Comment on the morphology of the erythrocytes.
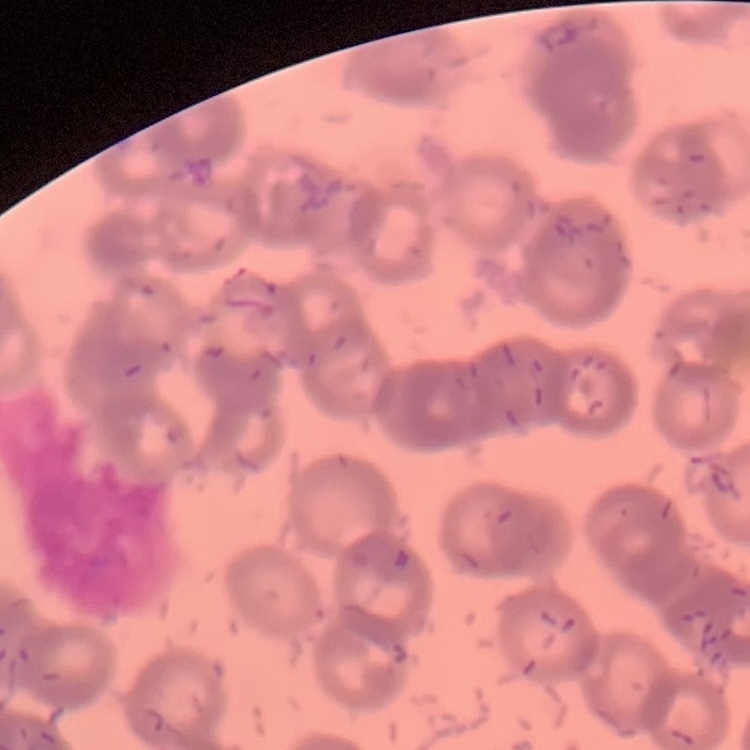
They show rouleaux formation.

Stained with either Field's or Giemsa. Square crop of a larger photomicrograph. Thin peripheral smear.